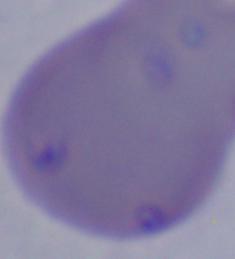

A Babesia parasite is seen. Captured at 1000x magnification. Photomicrograph.